State the blood parasite species.
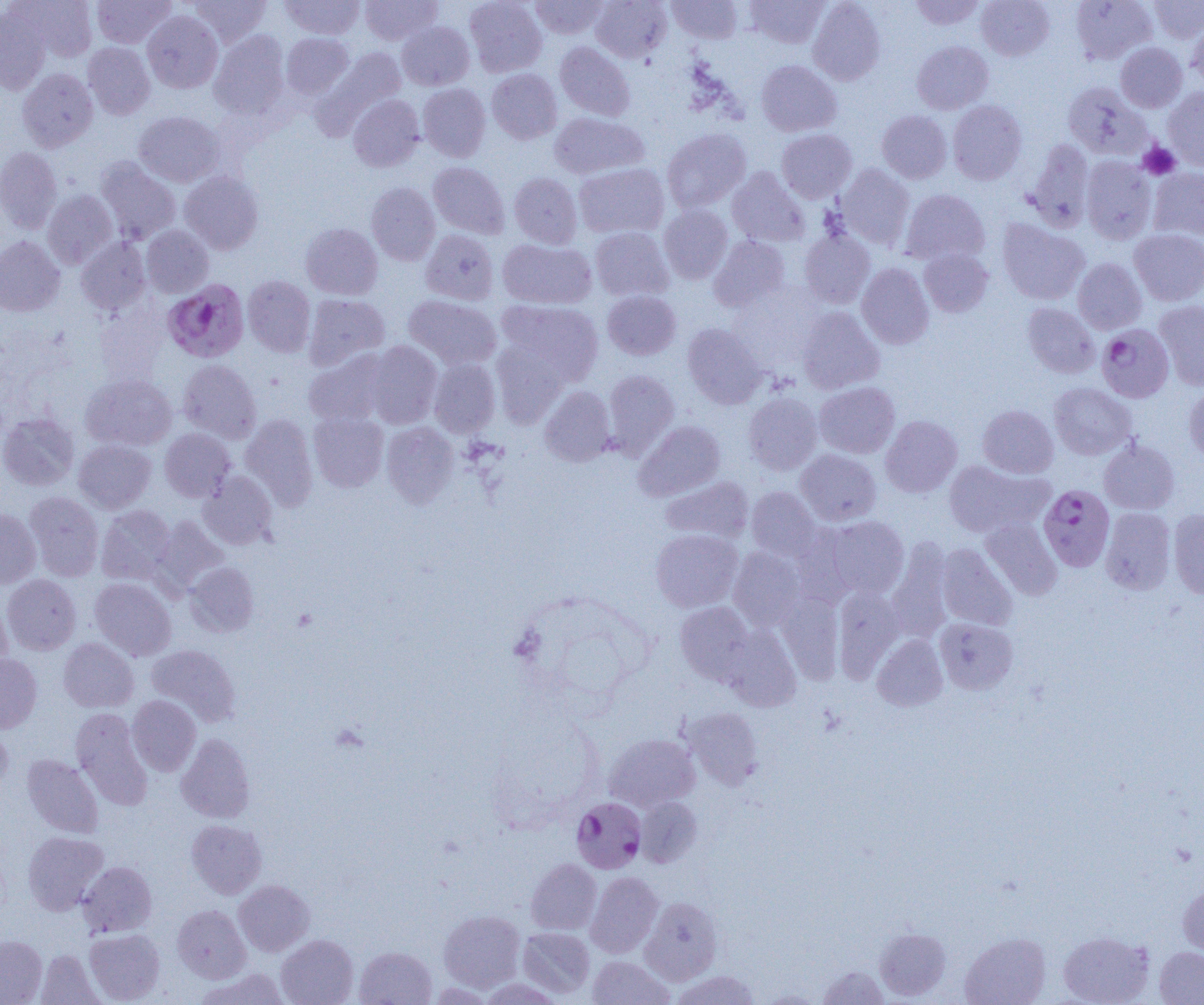

Plasmodium falciparum.

magnification = 1000x
modality = light microscopy
field of view = single
uninfected red blood cell locations = approximate bounding boxes as named x1/y1/x2/y2 corners in pixels: (x1=15, y1=0, x2=97, y2=61), (x1=92, y1=0, x2=175, y2=48), (x1=189, y1=0, x2=270, y2=47), (x1=280, y1=0, x2=365, y2=39), (x1=360, y1=0, x2=442, y2=46), (x1=464, y1=0, x2=546, y2=77), (x1=530, y1=0, x2=609, y2=39), (x1=591, y1=0, x2=672, y2=62), (x1=667, y1=0, x2=742, y2=44), (x1=743, y1=0, x2=830, y2=48), (x1=908, y1=0, x2=986, y2=30), (x1=976, y1=0, x2=1055, y2=61), (x1=1071, y1=0, x2=1157, y2=64), (x1=1148, y1=0, x2=1204, y2=43), (x1=807, y1=1, x2=886, y2=86), (x1=0, y1=8, x2=50, y2=94), (x1=142, y1=11, x2=223, y2=93), (x1=1186, y1=19, x2=1204, y2=92), (x1=397, y1=22, x2=474, y2=90), (x1=209, y1=31, x2=291, y2=120), (x1=281, y1=33, x2=353, y2=99), (x1=912, y1=41, x2=993, y2=114), (x1=555, y1=42, x2=635, y2=121), (x1=83, y1=43, x2=155, y2=119), (x1=1115, y1=43, x2=1187, y2=112), (x1=322, y1=46, x2=407, y2=128), (x1=755, y1=60, x2=842, y2=137), (x1=17, y1=68, x2=98, y2=152), (x1=486, y1=69, x2=562, y2=144), (x1=1062, y1=81, x2=1152, y2=160), (x1=417, y1=83, x2=491, y2=161), (x1=1163, y1=87, x2=1204, y2=171), (x1=348, y1=94, x2=424, y2=171), (x1=947, y1=100, x2=1027, y2=185), (x1=877, y1=110, x2=952, y2=183), (x1=134, y1=111, x2=224, y2=187), (x1=549, y1=112, x2=649, y2=179), (x1=662, y1=127, x2=751, y2=213), (x1=776, y1=129, x2=857, y2=203), (x1=1024, y1=139, x2=1095, y2=232), (x1=0, y1=147, x2=62, y2=233), (x1=1081, y1=156, x2=1157, y2=244), (x1=95, y1=157, x2=181, y2=244), (x1=428, y1=162, x2=510, y2=239), (x1=574, y1=163, x2=669, y2=239), (x1=834, y1=165, x2=915, y2=250), (x1=726, y1=167, x2=810, y2=247), (x1=1147, y1=167, x2=1204, y2=243), (x1=179, y1=171, x2=264, y2=254), (x1=509, y1=173, x2=582, y2=248), (x1=366, y1=182, x2=441, y2=265), (x1=900, y1=188, x2=990, y2=266), (x1=42, y1=190, x2=118, y2=268), (x1=658, y1=204, x2=733, y2=284), (x1=996, y1=218, x2=1090, y2=305), (x1=300, y1=223, x2=382, y2=300), (x1=141, y1=226, x2=213, y2=297), (x1=591, y1=227, x2=673, y2=301), (x1=799, y1=228, x2=875, y2=308), (x1=1129, y1=228, x2=1204, y2=306), (x1=420, y1=229, x2=498, y2=305), (x1=709, y1=235, x2=790, y2=312), (x1=0, y1=236, x2=65, y2=316), (x1=76, y1=237, x2=151, y2=315), (x1=497, y1=238, x2=595, y2=309), (x1=918, y1=248, x2=993, y2=317), (x1=1073, y1=258, x2=1147, y2=334), (x1=856, y1=263, x2=934, y2=349), (x1=243, y1=275, x2=316, y2=357), (x1=602, y1=290, x2=681, y2=360), (x1=303, y1=294, x2=390, y2=371), (x1=403, y1=295, x2=502, y2=370), (x1=496, y1=300, x2=603, y2=385), (x1=1154, y1=300, x2=1204, y2=390), (x1=1022, y1=302, x2=1100, y2=378), (x1=797, y1=307, x2=885, y2=394), (x1=682, y1=323, x2=767, y2=409), (x1=491, y1=340, x2=571, y2=428), (x1=365, y1=341, x2=443, y2=428), (x1=304, y1=351, x2=391, y2=426), (x1=429, y1=358, x2=500, y2=437), (x1=178, y1=360, x2=261, y2=444), (x1=602, y1=369, x2=679, y2=458), (x1=81, y1=374, x2=177, y2=451), (x1=814, y1=382, x2=900, y2=458), (x1=1049, y1=382, x2=1137, y2=460), (x1=1184, y1=384, x2=1204, y2=464), (x1=540, y1=386, x2=616, y2=466), (x1=743, y1=393, x2=822, y2=475), (x1=978, y1=405, x2=1058, y2=478), (x1=0, y1=412, x2=79, y2=490), (x1=308, y1=412, x2=388, y2=492), (x1=240, y1=414, x2=318, y2=510), (x1=880, y1=415, x2=962, y2=498), (x1=634, y1=420, x2=726, y2=501), (x1=381, y1=422, x2=458, y2=507), (x1=160, y1=428, x2=236, y2=501), (x1=1098, y1=438, x2=1179, y2=515), (x1=74, y1=439, x2=155, y2=513), (x1=796, y1=449, x2=882, y2=526), (x1=943, y1=460, x2=1054, y2=538), (x1=199, y1=471, x2=276, y2=548), (x1=661, y1=476, x2=753, y2=545), (x1=746, y1=487, x2=821, y2=561), (x1=25, y1=491, x2=104, y2=581), (x1=97, y1=505, x2=176, y2=584), (x1=1101, y1=507, x2=1177, y2=595), (x1=0, y1=509, x2=41, y2=588), (x1=1168, y1=509, x2=1204, y2=599), (x1=150, y1=516, x2=228, y2=595), (x1=820, y1=516, x2=910, y2=600), (x1=981, y1=517, x2=1062, y2=600), (x1=651, y1=529, x2=743, y2=612), (x1=886, y1=538, x2=955, y2=641), (x1=936, y1=543, x2=1018, y2=631), (x1=728, y1=547, x2=806, y2=631), (x1=184, y1=561, x2=259, y2=637), (x1=2, y1=574, x2=81, y2=655), (x1=90, y1=577, x2=176, y2=661), (x1=832, y1=586, x2=905, y2=682), (x1=777, y1=592, x2=845, y2=683), (x1=0, y1=595, x2=12, y2=672), (x1=675, y1=602, x2=757, y2=685), (x1=934, y1=617, x2=1018, y2=695), (x1=721, y1=625, x2=801, y2=712), (x1=872, y1=634, x2=948, y2=711), (x1=58, y1=638, x2=138, y2=712), (x1=146, y1=645, x2=241, y2=727), (x1=0, y1=653, x2=42, y2=733), (x1=127, y1=695, x2=201, y2=776), (x1=682, y1=706, x2=764, y2=790), (x1=71, y1=708, x2=152, y2=810), (x1=0, y1=726, x2=13, y2=795), (x1=176, y1=733, x2=255, y2=823), (x1=604, y1=733, x2=700, y2=812), (x1=22, y1=754, x2=104, y2=838), (x1=635, y1=796, x2=703, y2=868), (x1=186, y1=819, x2=266, y2=898), (x1=22, y1=831, x2=108, y2=915), (x1=526, y1=858, x2=602, y2=934), (x1=78, y1=861, x2=157, y2=937), (x1=585, y1=871, x2=663, y2=958), (x1=234, y1=880, x2=315, y2=956), (x1=1178, y1=881, x2=1204, y2=959), (x1=639, y1=895, x2=723, y2=984), (x1=172, y1=905, x2=251, y2=983), (x1=438, y1=909, x2=526, y2=992), (x1=517, y1=926, x2=595, y2=998), (x1=875, y1=928, x2=951, y2=1001), (x1=84, y1=929, x2=165, y2=1004), (x1=1058, y1=931, x2=1154, y2=1005), (x1=960, y1=932, x2=1051, y2=1005), (x1=276, y1=934, x2=358, y2=1005), (x1=0, y1=935, x2=47, y2=1004), (x1=355, y1=946, x2=436, y2=1005), (x1=1155, y1=946, x2=1204, y2=1004), (x1=36, y1=950, x2=104, y2=1005), (x1=587, y1=955, x2=674, y2=1005), (x1=817, y1=965, x2=889, y2=1004), (x1=197, y1=967, x2=290, y2=1005), (x1=671, y1=970, x2=763, y2=1004)
platelet locations = approximate bounding boxes as named x1/y1/x2/y2 corners in pixels: (x1=1138, y1=142, x2=1181, y2=180)
image size = 1204×1005 pixels
Plasmodium falciparum-infected red blood cell locations = approximate bounding boxes as named x1/y1/x2/y2 corners in pixels: (x1=163, y1=279, x2=249, y2=362), (x1=1096, y1=323, x2=1174, y2=403), (x1=1038, y1=485, x2=1115, y2=571), (x1=571, y1=797, x2=647, y2=873)
preparation = thin blood film